Describe the morphology of the erythrocytes.
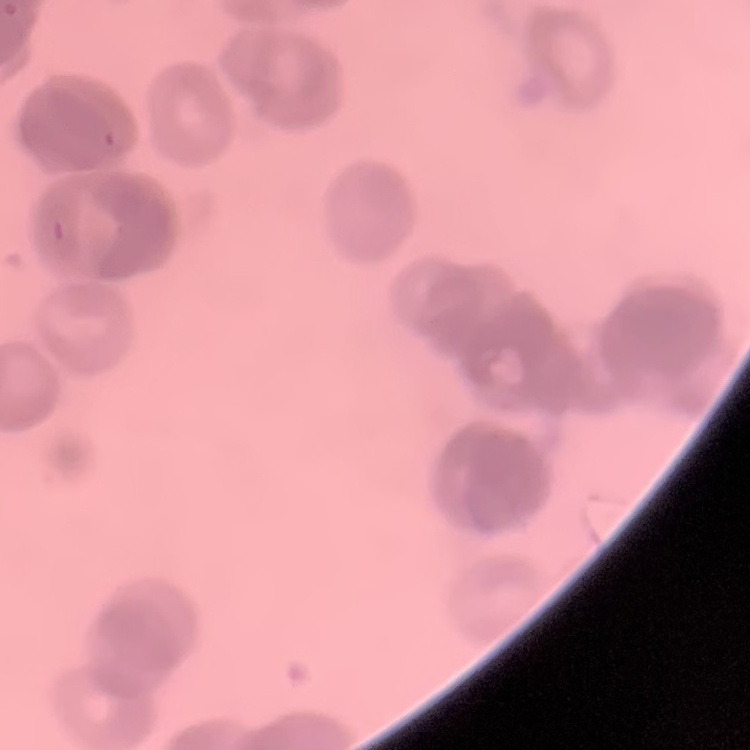
They show rouleaux formation.

Summary:
  - Image type: one tile cut from a larger photomicrograph
  - Preparation: thin blood smear
  - Stain: Field's or Giemsa